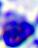 400x magnification. A white blood cell is shown. Micrograph.